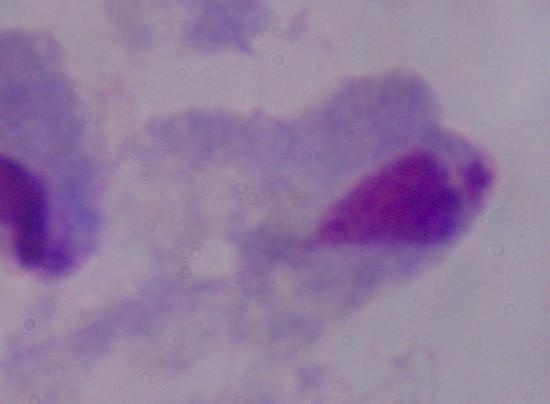 Photomicrograph. A trichomonad is seen. 1000x magnification.